Locate malaria parasites and leukocytes.
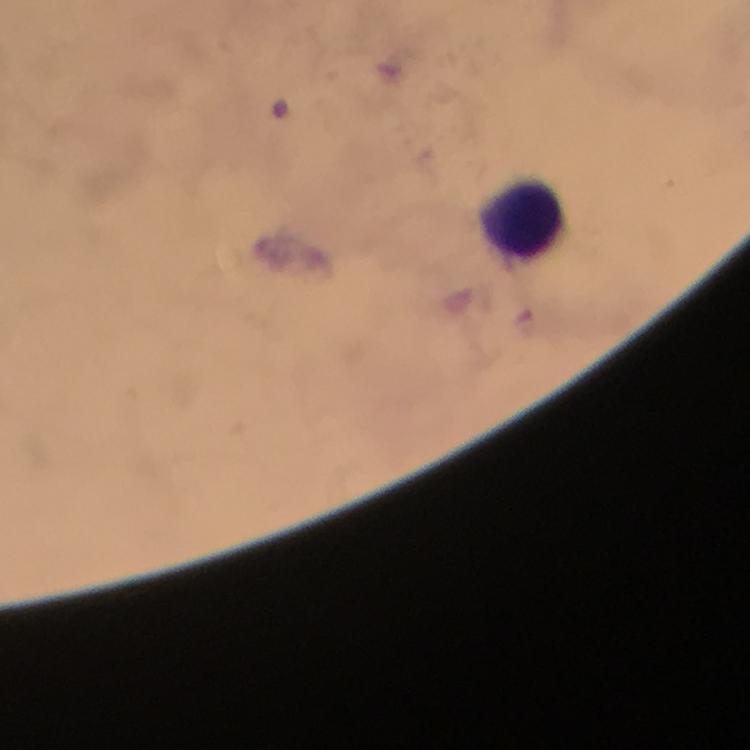
No malaria parasites detected.
Approximate centers as (x, y) in pixels.
Leukocytes: (521, 215).

Summary:
  - Stain: Giemsa
  - Preparation: thick blood film
  - Magnification: 100x
  - Image size: 750×750 pixels
  - Immersion oil: used
  - Context: from a diagnostic examination for malaria
  - Cropped from: a single field of view
  - Capture: smartphone photograph through a microscope